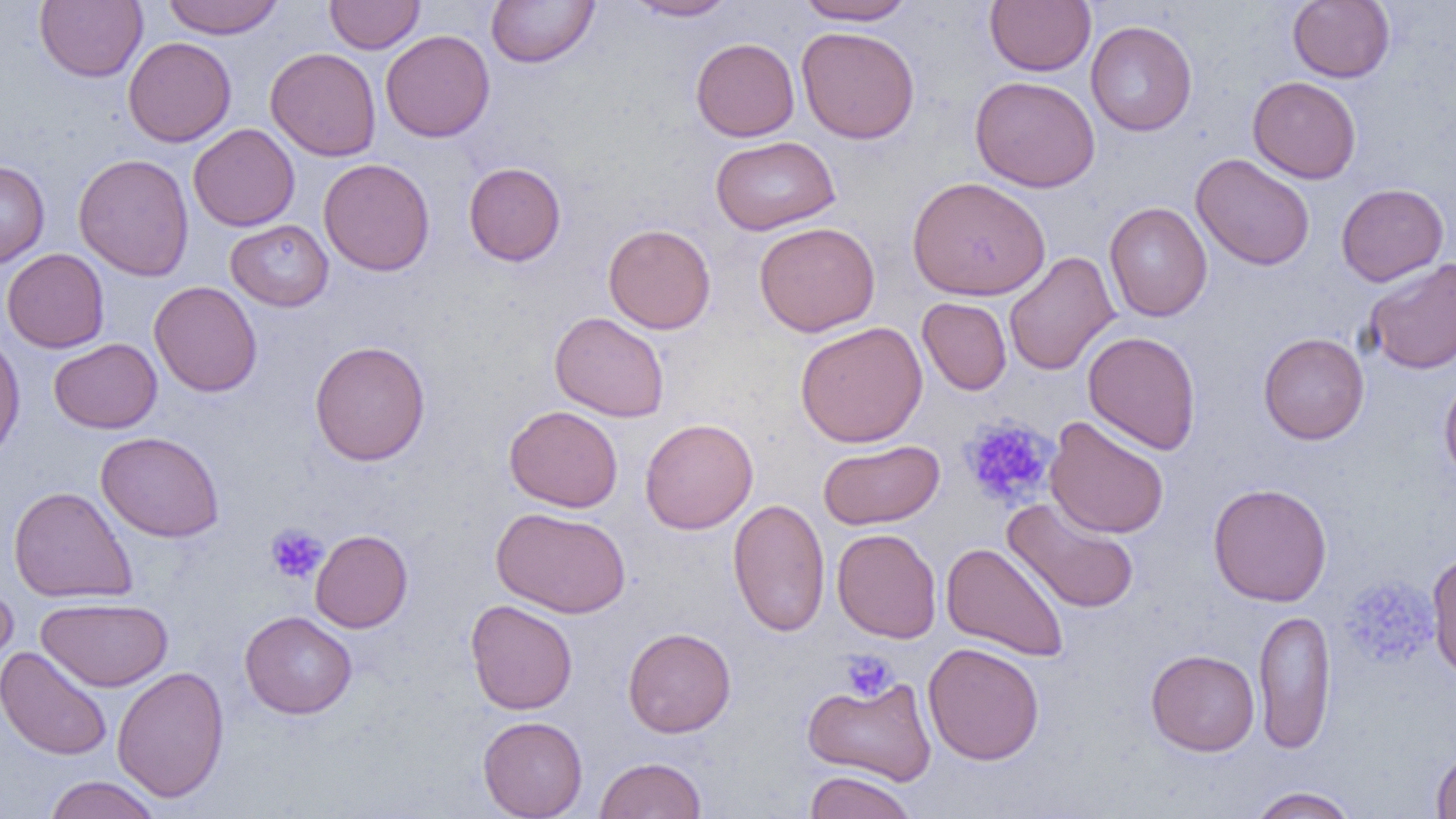

slide-level diagnosis = no evidence of blood parasites
preparation = thin blood smear
modality = light microscopy
field of view = single
magnification = 1000x
image size = 1456×819 pixels
platelet locations = approximate bounding boxes as [x1, y1, x2, y2] in pixels: [958, 415, 1057, 510], [266, 523, 328, 584], [1339, 575, 1439, 669], [839, 649, 898, 702]
uninfected red blood cell locations = approximate bounding boxes as [x1, y1, x2, y2] in pixels: [34, 0, 147, 82], [161, 0, 286, 38], [324, 0, 425, 54], [486, 0, 599, 68], [624, 0, 738, 21], [984, 0, 1096, 76], [1287, 0, 1395, 83], [795, 1, 917, 25], [1086, 20, 1197, 136], [796, 26, 920, 143], [380, 29, 495, 142], [123, 37, 236, 147], [690, 37, 799, 142], [265, 47, 381, 161], [970, 76, 1100, 192], [1247, 76, 1361, 184], [188, 123, 300, 231], [710, 135, 841, 235], [73, 153, 194, 281], [1191, 153, 1315, 271], [318, 158, 435, 277], [0, 160, 50, 268], [463, 161, 566, 266], [906, 176, 1051, 301], [1336, 183, 1449, 286], [1104, 202, 1213, 322], [225, 219, 334, 311], [754, 222, 880, 336], [603, 223, 716, 334], [1, 248, 110, 353], [1004, 251, 1119, 376], [1363, 257, 1456, 374], [149, 281, 262, 397], [917, 297, 1012, 395], [549, 311, 670, 422], [794, 321, 928, 448], [1082, 330, 1202, 455], [0, 332, 25, 461], [1258, 332, 1370, 444], [49, 338, 162, 433], [309, 340, 431, 466], [1439, 372, 1456, 486], [504, 405, 623, 512], [1044, 416, 1170, 539], [640, 417, 758, 534], [96, 431, 224, 542], [817, 439, 944, 530], [1207, 483, 1332, 607], [8, 486, 138, 604], [728, 497, 830, 637], [1002, 497, 1141, 614], [491, 506, 631, 619], [832, 527, 942, 643], [310, 529, 413, 633], [940, 542, 1070, 662], [1426, 549, 1456, 680], [0, 579, 18, 683], [36, 596, 174, 692], [465, 599, 577, 715], [1253, 608, 1337, 755], [240, 611, 357, 719], [623, 627, 736, 737], [922, 642, 1044, 765], [0, 645, 113, 761], [1146, 649, 1260, 756], [111, 666, 229, 803], [802, 676, 938, 785], [477, 715, 588, 818], [1430, 747, 1456, 818], [595, 756, 707, 819], [803, 770, 919, 819], [43, 775, 163, 819], [1247, 786, 1359, 818]